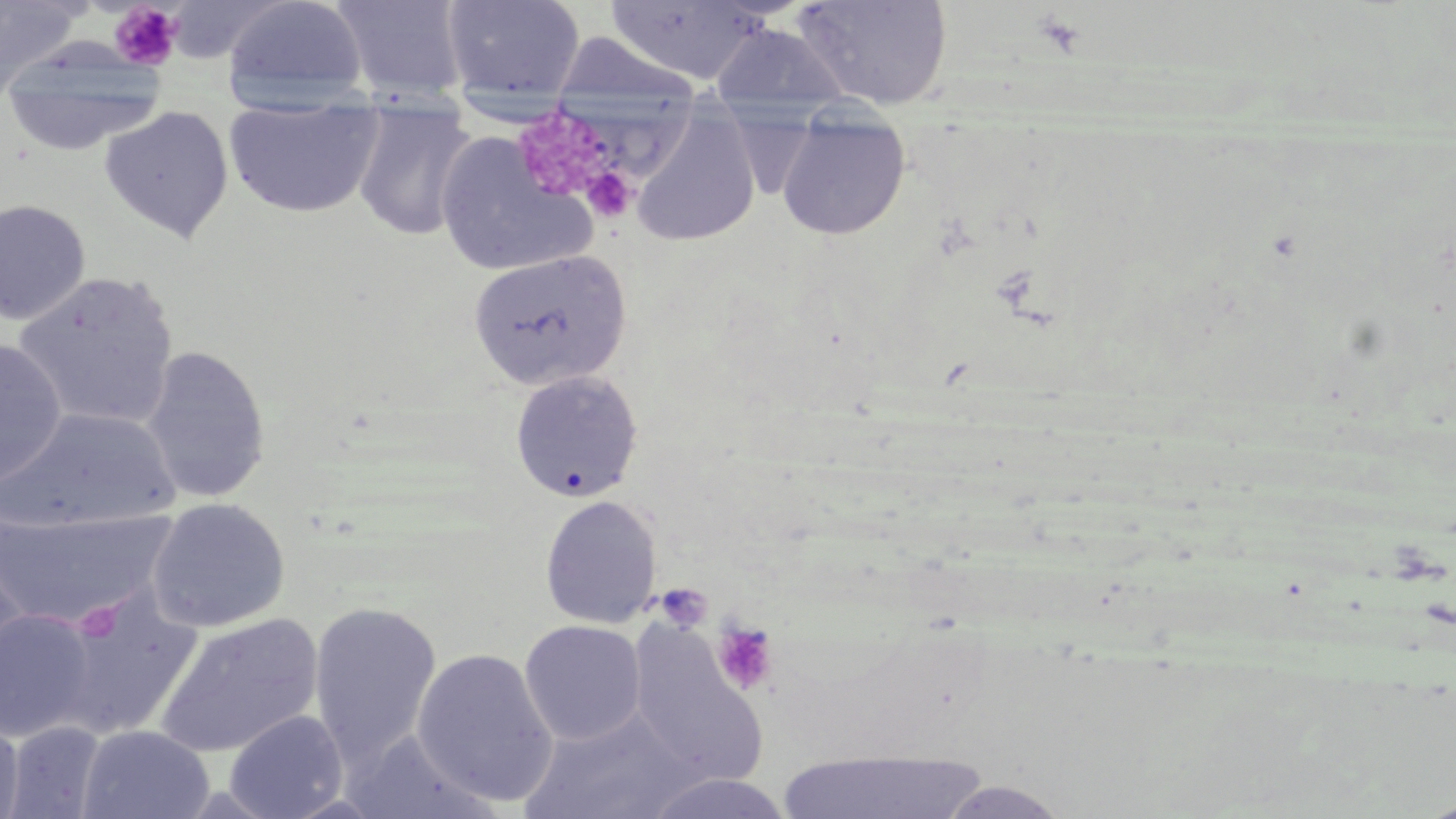
slide_level_diagnosis: negative for blood parasites
field_of_view: single
uninfected_red_blood_cell_locations: 'approximate bounding boxes as [x1, y1, x2, y2] in pixels: [0, 0, 83, 89], [221, 0, 369, 110], [441, 0, 586, 101], [791, 0, 952, 110], [330, 1, 470, 103], [604, 1, 772, 87], [710, 23, 852, 120], [548, 31, 704, 106], [1, 47, 164, 157], [224, 99, 384, 219], [351, 101, 476, 242], [99, 106, 234, 243], [631, 110, 761, 248], [775, 110, 911, 240], [436, 130, 596, 278], [0, 199, 91, 325], [467, 249, 631, 390], [13, 271, 180, 432], [0, 337, 67, 492], [140, 345, 272, 503], [509, 370, 644, 503], [1, 407, 181, 535], [539, 495, 663, 629], [146, 498, 290, 633], [0, 504, 176, 629], [1, 558, 32, 694], [52, 588, 202, 740], [308, 602, 442, 768], [0, 608, 98, 743], [154, 613, 325, 758], [519, 620, 647, 745], [625, 625, 767, 786], [411, 647, 559, 808], [520, 709, 702, 819], [223, 710, 348, 819], [0, 714, 24, 819], [5, 720, 107, 817], [77, 725, 214, 819], [771, 748, 993, 818], [640, 772, 797, 818], [935, 779, 1073, 818]'
magnification: 1000x
modality: light microscopy
platelet_locations: 'approximate bounding boxes as [x1, y1, x2, y2] in pixels: [109, 3, 184, 71], [1032, 11, 1087, 58], [581, 166, 637, 222], [656, 583, 713, 631], [711, 620, 780, 696]'
image_size: 1456×819 pixels
preparation: thin blood film
stain: May-Grünwald-Giemsa